Name the parasite shown.
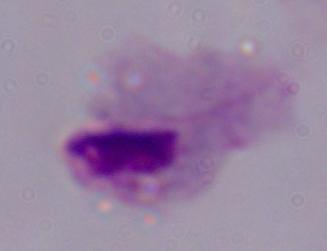

This is a trichomonad.

Photomicrograph. Captured at 1000x magnification.